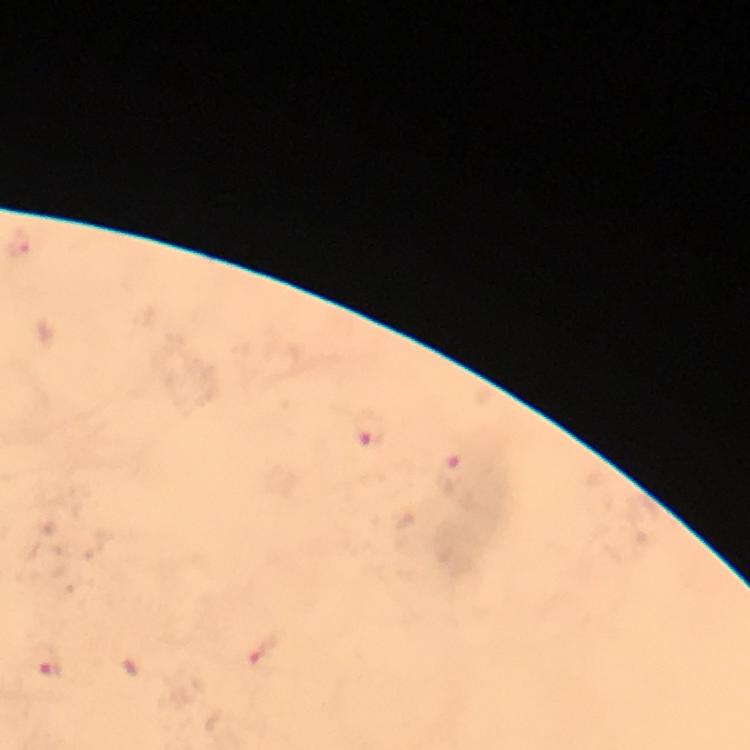
{
  "plasmodium_parasite_locations": "approximate centers as (x, y) in pixels: (18, 243), (371, 428), (452, 472), (263, 651), (50, 663)",
  "cropped_from": "a single field of view",
  "context": "from a diagnostic examination for malaria",
  "capture": "smartphone camera through the microscope",
  "image_size": "750×750 pixels",
  "immersion_oil": "applied",
  "stain": "Giemsa",
  "preparation": "thick blood film",
  "magnification": "100x"
}